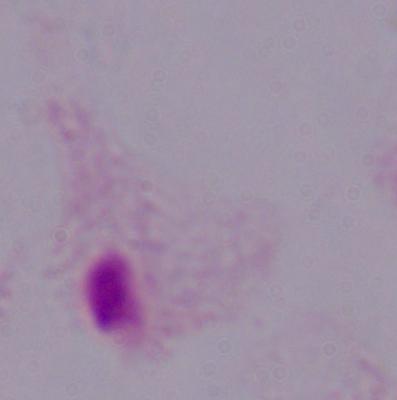
modality: photomicrograph
identification: trichomonad
magnification: 1000x